Describe the morphology of the erythrocytes.
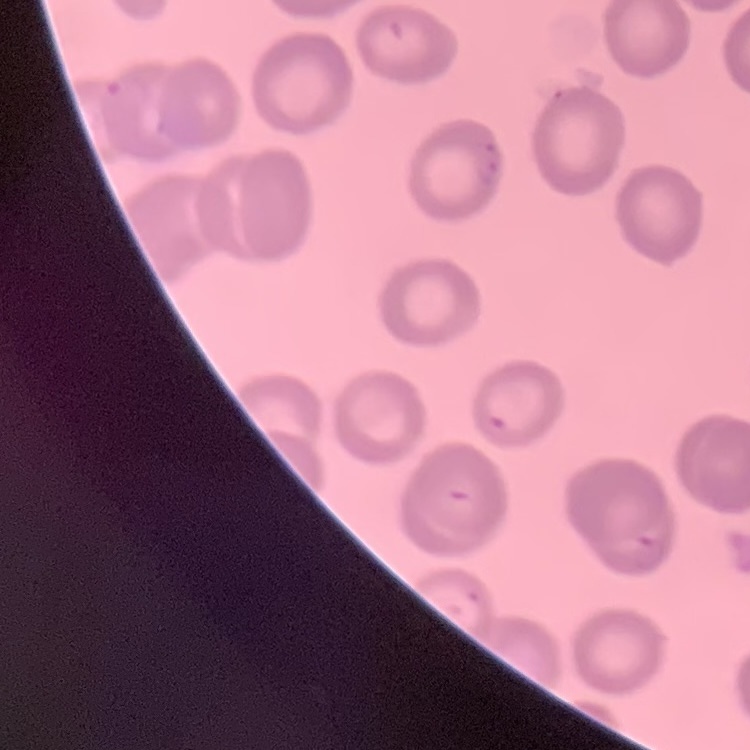

No rouleaux formation.

Field's or Giemsa stain. One tile cut from a larger photomicrograph. Thin blood film.